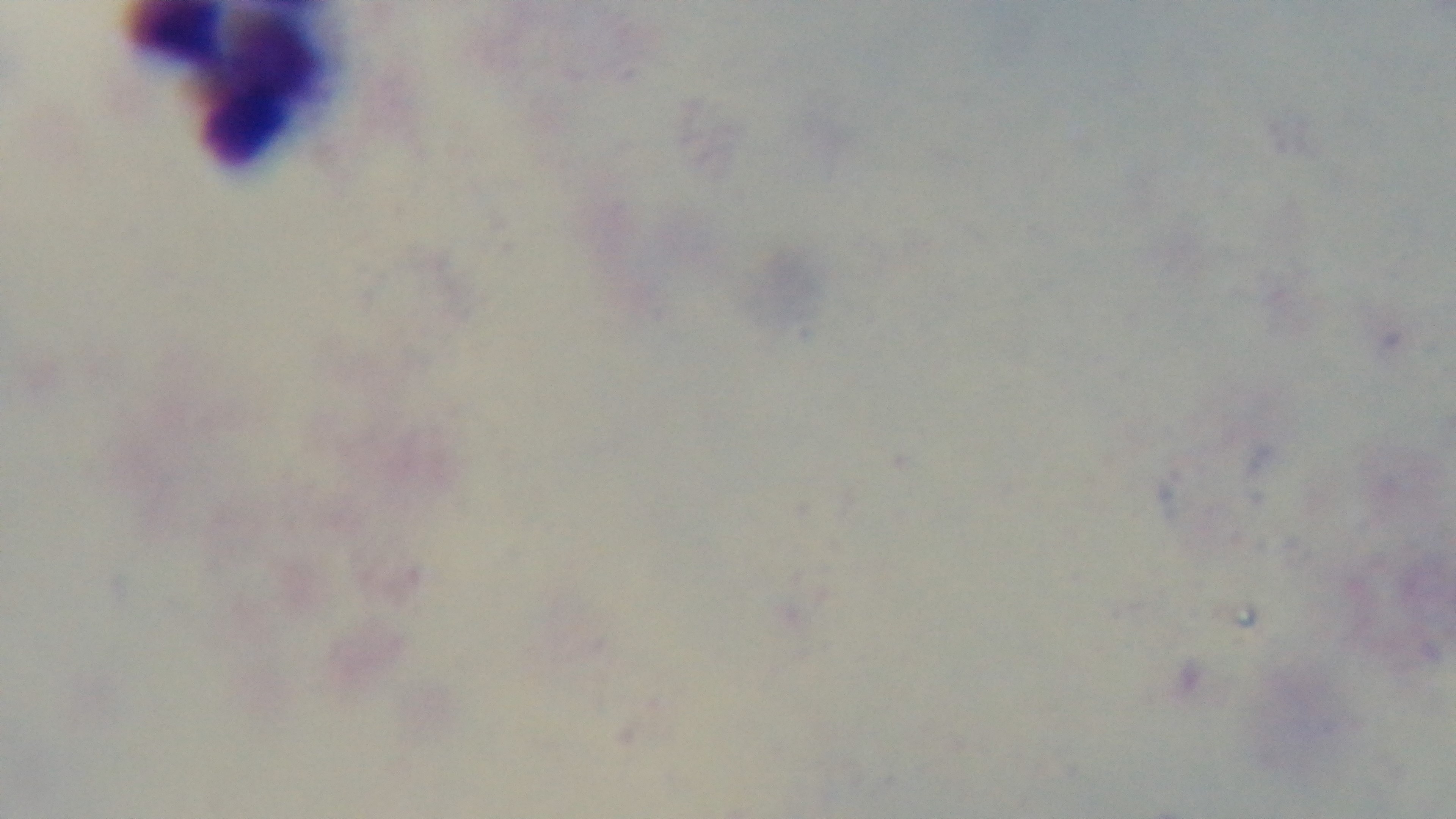
Summary:
  - Objective: 100x oil immersion
  - Modality: light microscopy
  - Preparation: thick
  - Stain: Giemsa
  - Capture: mounted 4K digital camera
  - Malaria status: negative
  - Field of view: one from the slide